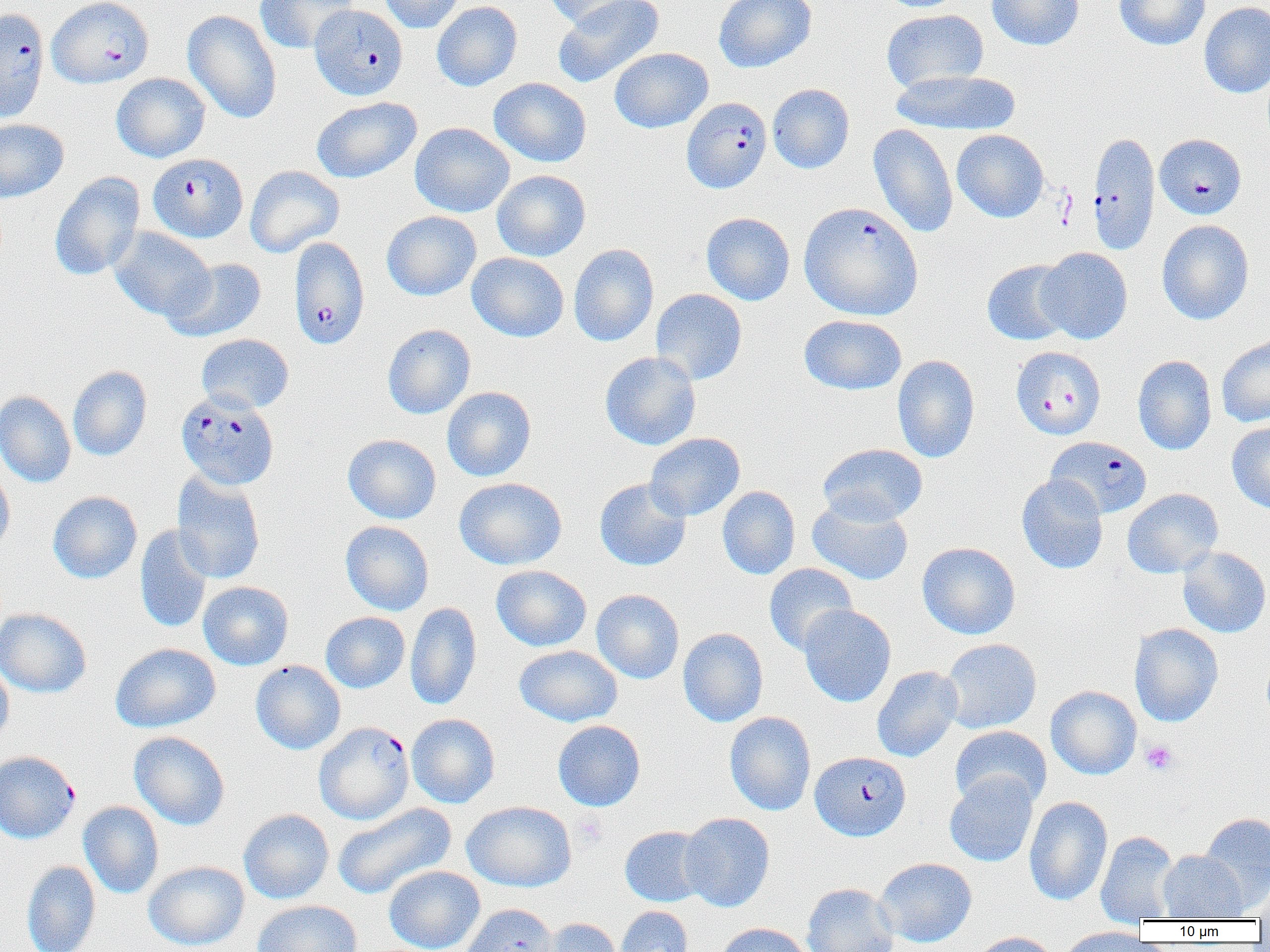

Summary:
  - Coordinate format: approximate bounding boxes as [x1, y1, x2, y2] in pixels
  - Plasmodium falciparum-infected red blood cell locations: [47, 0, 154, 88], [309, 4, 408, 101], [0, 7, 49, 123], [682, 97, 771, 194], [1088, 132, 1160, 255], [1154, 133, 1246, 220], [148, 152, 247, 243], [799, 201, 923, 320], [288, 236, 370, 349], [1011, 346, 1106, 440], [175, 390, 279, 490], [1046, 436, 1152, 519], [320, 724, 420, 827], [810, 751, 911, 841], [2, 753, 81, 847]
  - Platelet locations: [1140, 740, 1179, 775], [573, 811, 608, 848]
  - Uninfected red blood cell locations: [255, 0, 358, 53], [378, 0, 466, 33], [541, 0, 643, 29], [552, 0, 665, 87], [714, 0, 816, 73], [877, 0, 968, 12], [986, 0, 1084, 51], [1114, 0, 1211, 50], [432, 1, 522, 91], [1199, 1, 1270, 99], [881, 9, 989, 93], [182, 10, 282, 124], [610, 47, 713, 133], [890, 69, 1021, 135], [111, 73, 211, 162], [489, 77, 591, 167], [767, 83, 854, 174], [311, 96, 422, 183], [0, 119, 69, 202], [410, 122, 514, 217], [868, 123, 958, 238], [951, 129, 1049, 222], [245, 166, 344, 257], [492, 170, 590, 262], [50, 171, 145, 281], [381, 211, 481, 301], [701, 212, 795, 305], [1156, 219, 1254, 325], [109, 226, 215, 321], [569, 243, 659, 346], [1037, 247, 1133, 344], [467, 252, 569, 342], [162, 257, 267, 343], [982, 259, 1074, 346], [650, 289, 747, 385], [799, 315, 907, 395], [382, 324, 475, 419], [196, 334, 294, 413], [1217, 335, 1270, 427], [599, 351, 701, 451], [892, 354, 980, 463], [1133, 355, 1217, 455], [68, 365, 152, 461], [442, 386, 536, 481], [0, 390, 76, 487], [1227, 421, 1270, 513], [645, 433, 745, 521], [343, 434, 441, 524], [818, 443, 928, 526], [0, 464, 15, 556], [172, 472, 266, 584], [1017, 473, 1108, 574], [454, 477, 567, 570], [594, 478, 691, 571], [717, 486, 800, 580], [1122, 488, 1223, 578], [47, 491, 142, 584], [807, 495, 913, 585], [340, 521, 434, 615], [134, 526, 212, 633], [917, 541, 1021, 639], [1177, 546, 1270, 638], [764, 563, 858, 656], [491, 565, 592, 651], [198, 581, 293, 670], [591, 589, 684, 683], [405, 602, 482, 710], [798, 605, 896, 707], [0, 608, 91, 697], [320, 612, 410, 693], [1129, 623, 1224, 727], [678, 628, 768, 727], [941, 638, 1042, 733], [110, 642, 221, 733], [514, 646, 623, 727], [250, 660, 346, 754], [0, 661, 13, 750], [871, 665, 963, 762], [1046, 685, 1142, 779], [724, 712, 816, 816], [406, 714, 500, 808], [552, 720, 645, 811], [950, 725, 1052, 810], [129, 731, 230, 830], [944, 772, 1038, 867], [1024, 796, 1113, 906], [78, 801, 164, 898], [462, 801, 577, 892], [332, 803, 457, 900], [238, 809, 334, 903], [679, 812, 775, 912], [1197, 812, 1270, 909], [620, 826, 710, 907], [1095, 831, 1179, 924], [1158, 850, 1247, 921], [875, 857, 976, 948], [21, 860, 101, 952], [143, 861, 249, 951], [384, 865, 485, 952], [1255, 877, 1270, 925], [802, 883, 899, 952], [252, 900, 362, 952], [460, 903, 559, 952], [616, 906, 693, 952], [535, 917, 624, 952], [714, 922, 813, 952], [1055, 926, 1152, 952], [969, 932, 1059, 952]
  - Slide-level diagnosis: Plasmodium falciparum
  - Image size: 1270×952 pixels
  - Modality: optical microscopy
  - Magnification: 1000x
  - Preparation: thin blood smear
  - Field of view: single